Name the blood parasite species.
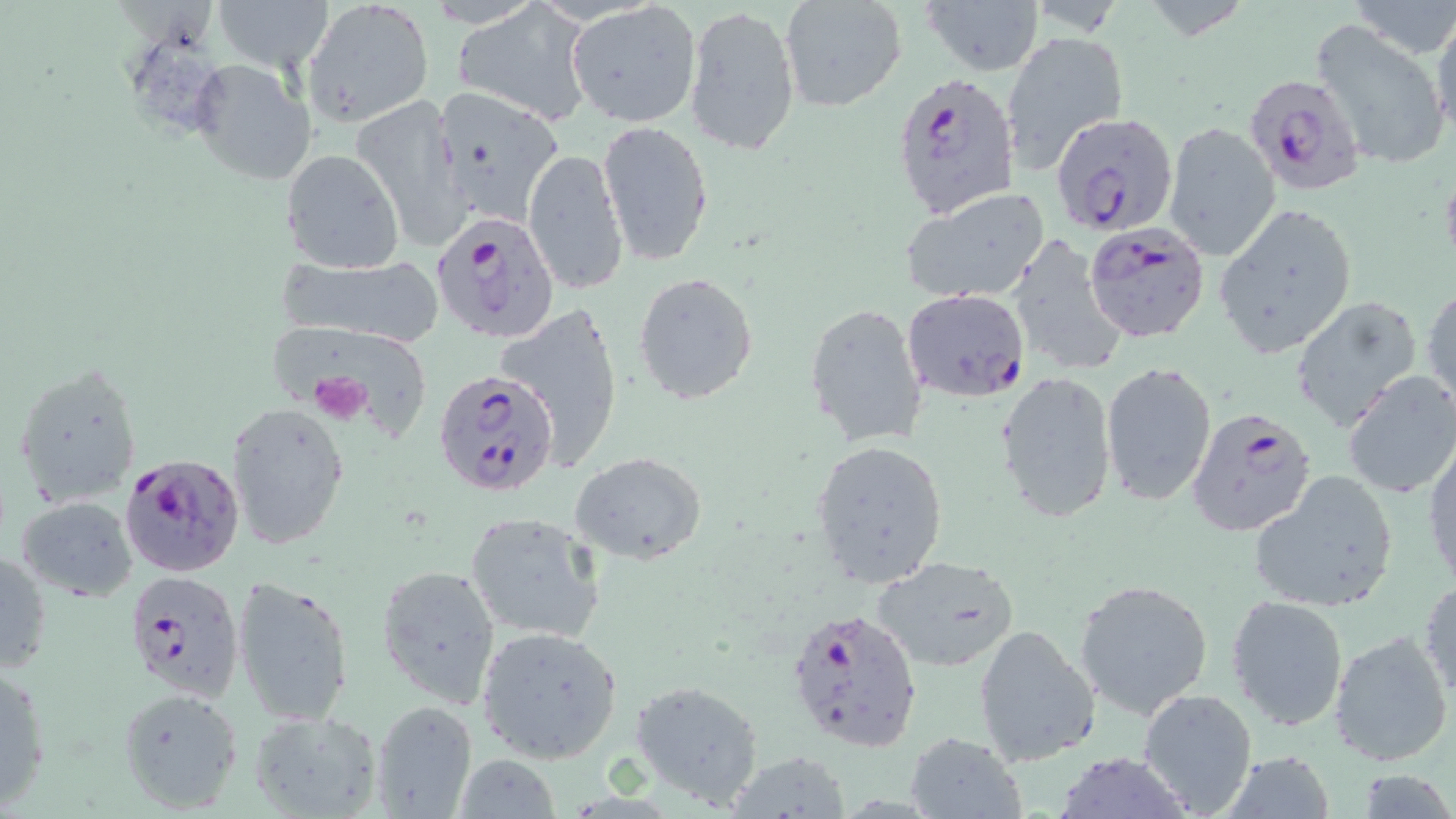
Plasmodium falciparum.

Summary:
  - Coordinate format: approximate bounding boxes as named x1/y1/x2/y2 corners in pixels
  - Platelet locations: (x1=306, y1=378, x2=378, y2=425)
  - Plasmodium falciparum-infected red blood cell locations: (x1=1242, y1=72, x2=1368, y2=197), (x1=891, y1=73, x2=1020, y2=221), (x1=1050, y1=111, x2=1177, y2=237), (x1=432, y1=210, x2=561, y2=343), (x1=1086, y1=221, x2=1210, y2=344), (x1=902, y1=288, x2=1030, y2=401), (x1=433, y1=369, x2=562, y2=498), (x1=1187, y1=407, x2=1317, y2=536), (x1=118, y1=450, x2=245, y2=579), (x1=124, y1=569, x2=245, y2=702), (x1=785, y1=605, x2=924, y2=753)
  - Uninfected red blood cell locations: (x1=216, y1=0, x2=332, y2=72), (x1=302, y1=0, x2=435, y2=130), (x1=778, y1=0, x2=909, y2=114), (x1=921, y1=0, x2=1042, y2=75), (x1=1347, y1=0, x2=1456, y2=61), (x1=566, y1=3, x2=701, y2=129), (x1=453, y1=4, x2=593, y2=126), (x1=684, y1=4, x2=801, y2=157), (x1=1431, y1=9, x2=1456, y2=144), (x1=1308, y1=19, x2=1450, y2=171), (x1=1002, y1=31, x2=1128, y2=176), (x1=187, y1=57, x2=316, y2=187), (x1=432, y1=88, x2=571, y2=227), (x1=350, y1=93, x2=470, y2=246), (x1=597, y1=120, x2=714, y2=266), (x1=1163, y1=121, x2=1281, y2=262), (x1=523, y1=146, x2=630, y2=293), (x1=281, y1=149, x2=405, y2=274), (x1=900, y1=187, x2=1049, y2=305), (x1=1214, y1=206, x2=1358, y2=358), (x1=1007, y1=236, x2=1125, y2=375), (x1=273, y1=253, x2=446, y2=347), (x1=633, y1=271, x2=759, y2=404), (x1=1422, y1=280, x2=1455, y2=415), (x1=1288, y1=294, x2=1423, y2=432), (x1=804, y1=301, x2=928, y2=450), (x1=269, y1=328, x2=436, y2=441), (x1=14, y1=360, x2=143, y2=504), (x1=1100, y1=361, x2=1216, y2=508), (x1=995, y1=370, x2=1117, y2=525), (x1=1340, y1=370, x2=1456, y2=501), (x1=224, y1=401, x2=350, y2=552), (x1=810, y1=439, x2=949, y2=589), (x1=1424, y1=440, x2=1456, y2=592), (x1=572, y1=452, x2=708, y2=564), (x1=1247, y1=472, x2=1400, y2=612), (x1=16, y1=495, x2=140, y2=601), (x1=464, y1=512, x2=604, y2=644), (x1=0, y1=546, x2=51, y2=678), (x1=872, y1=555, x2=1021, y2=672), (x1=376, y1=562, x2=502, y2=710), (x1=232, y1=576, x2=356, y2=733), (x1=1074, y1=577, x2=1214, y2=719), (x1=1418, y1=579, x2=1455, y2=702), (x1=1226, y1=594, x2=1349, y2=732), (x1=973, y1=623, x2=1102, y2=766), (x1=476, y1=624, x2=624, y2=762), (x1=1329, y1=628, x2=1454, y2=766), (x1=0, y1=660, x2=51, y2=812), (x1=628, y1=678, x2=765, y2=809), (x1=117, y1=686, x2=245, y2=812), (x1=1137, y1=687, x2=1258, y2=817), (x1=370, y1=701, x2=479, y2=817), (x1=247, y1=709, x2=384, y2=819), (x1=905, y1=731, x2=1025, y2=818), (x1=1052, y1=751, x2=1194, y2=818), (x1=1221, y1=751, x2=1341, y2=817), (x1=724, y1=752, x2=850, y2=817), (x1=453, y1=755, x2=561, y2=819)
  - Stain: May-Grünwald-Giemsa
  - Modality: optical microscopy
  - Preparation: thin blood film
  - Image size: 1456×819 pixels
  - Field of view: one of a larger specimen
  - Magnification: 1000x